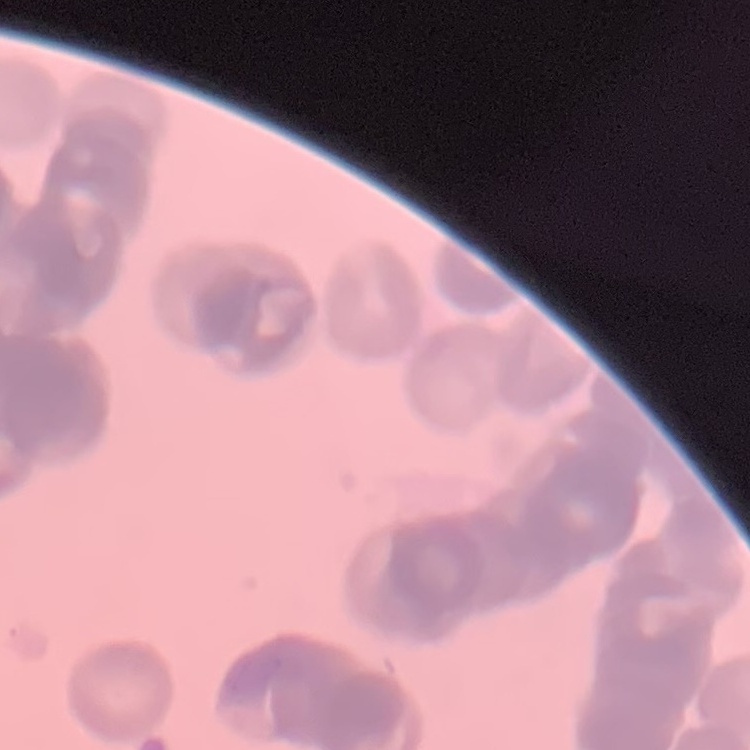

Summary:
  - Red blood cell morphology: rouleaux formation
  - Stain: Field's or Giemsa
  - Preparation: thin peripheral smear
  - Image type: square crop of a larger photomicrograph